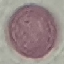
Summary:
  - Result: no malaria parasites seen
  - Stain: Giemsa
  - Preparation: thin smear
  - Capture: smartphone camera at the microscope eyepiece
  - Image type: automatically extracted cell patch, resized to 64 × 64 pixels